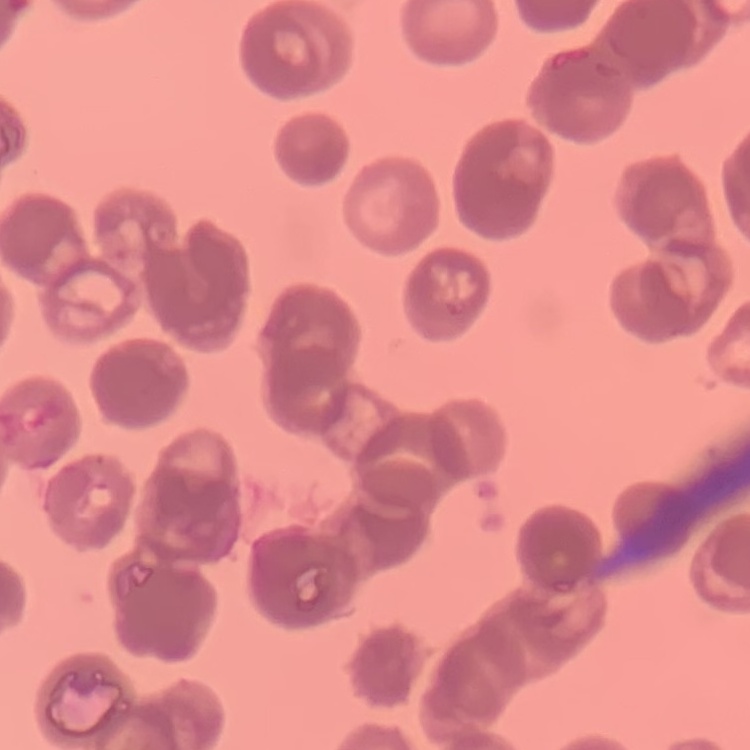
Summary:
  - Red blood cell morphology: rouleaux formation
  - Preparation: thin blood smear
  - Stain: Field's or Giemsa
  - Image type: one tile cut from a larger photomicrograph